Look for parasitized red blood cells.
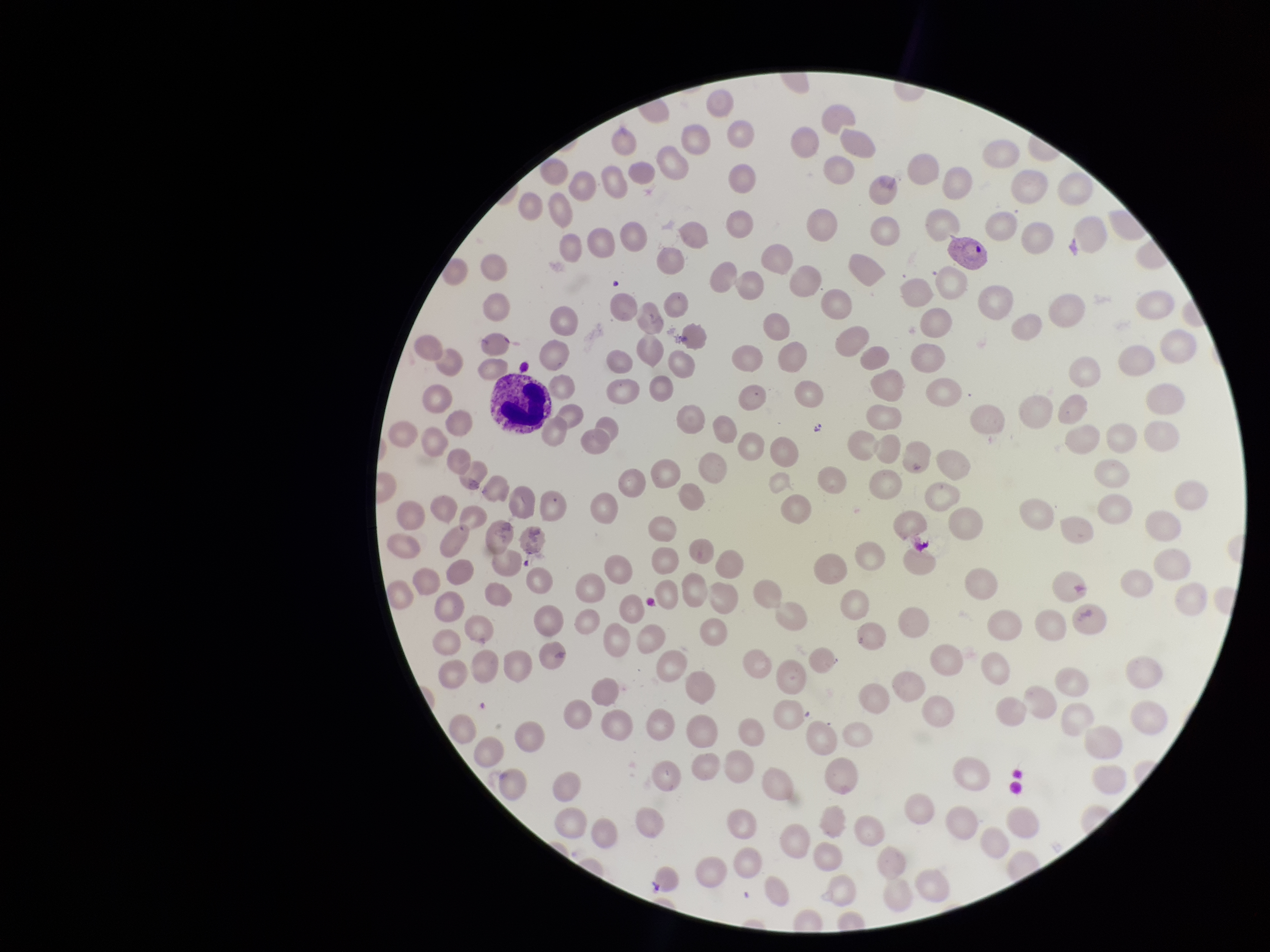
Detected.

red blood cell count = 187
preparation = thin blood smear
stain = Giemsa
species reported for this patient = Plasmodium vivax
patient malaria status = infected
capture = smartphone photograph through the microscope eyepiece
parasitized red blood cell count = 1
field of view = one from this slide
image size = 1270×952 pixels